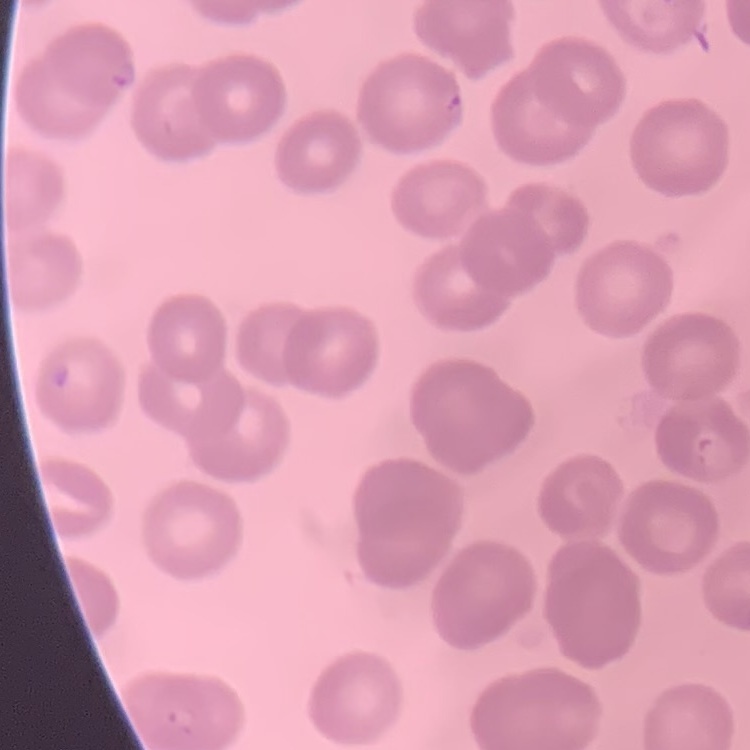

red blood cell morphology = no rouleaux formation
preparation = thin blood film
image type = one tile cut from a larger photomicrograph
stain = Field's or Giemsa